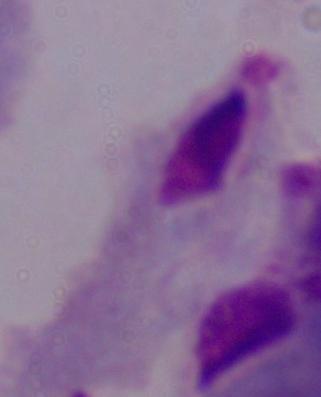

1000x magnification. Micrograph. A trichomonad is seen.